Classify this cell by malaria status.
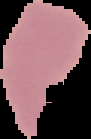
Uninfected.

Summary:
  - Preparation: thin blood smear
  - Image size: 91×139 pixels
  - Image type: segmented cell region with the area outside set to black